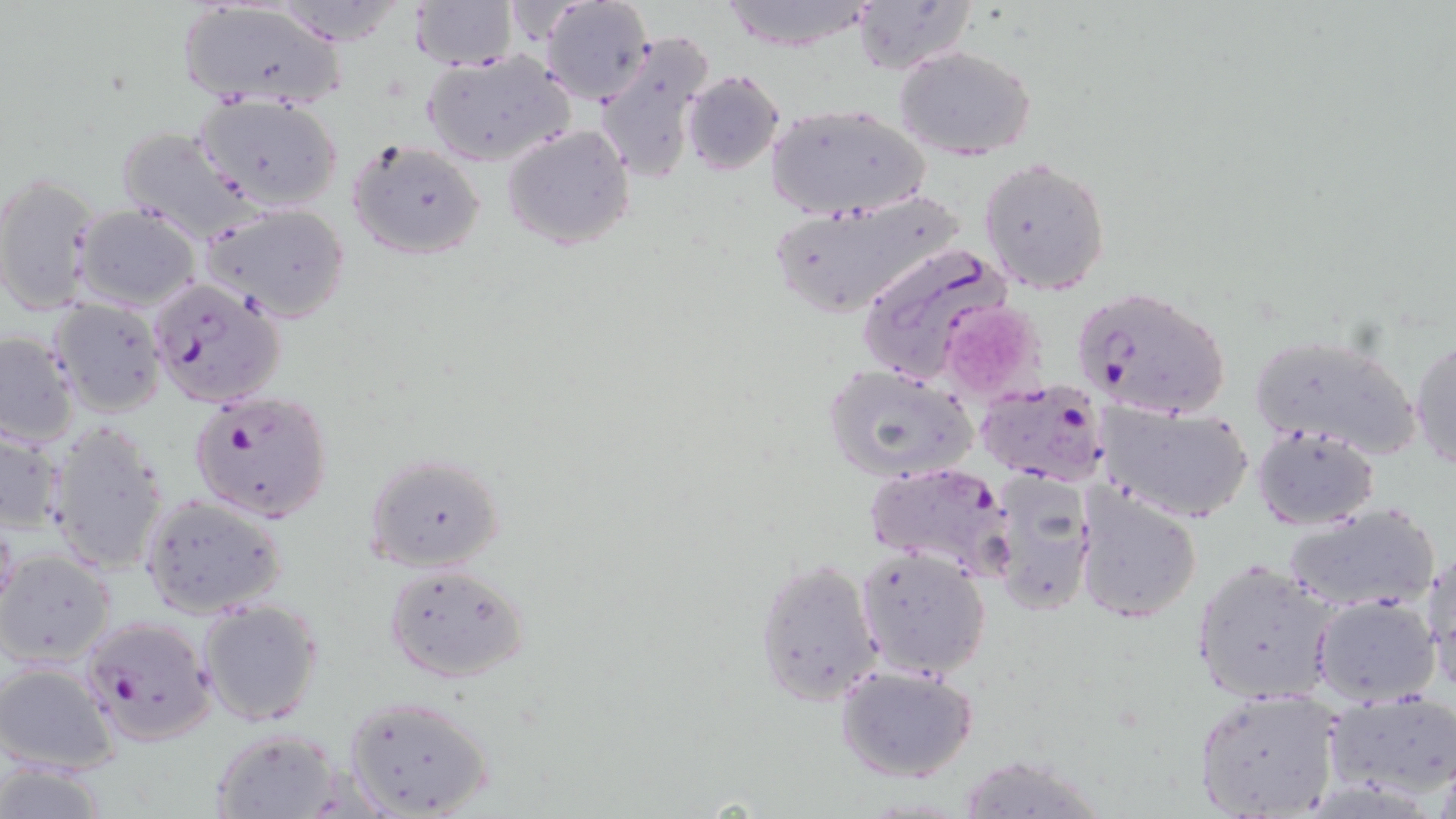 Approximate bounding boxes as [x1, y1, x2, y2] in pixels. Plasmodium falciparum-infected red blood cell locations: [855, 243, 1016, 392], [146, 277, 285, 409], [1073, 285, 1231, 423], [977, 379, 1111, 488], [189, 388, 334, 524], [864, 463, 1017, 581], [76, 615, 217, 745]. Platelet locations: [939, 299, 1049, 402]. Uninfected red blood cell locations: [269, 0, 411, 48], [539, 0, 654, 105], [719, 0, 875, 52], [174, 1, 347, 110], [408, 1, 519, 69], [502, 1, 592, 44], [851, 1, 979, 75], [593, 30, 716, 185], [894, 46, 1037, 161], [421, 49, 575, 168], [680, 70, 785, 175], [197, 94, 344, 210], [765, 104, 929, 221], [502, 124, 636, 251], [114, 126, 259, 242], [346, 138, 486, 262], [978, 158, 1111, 297], [0, 171, 98, 317], [763, 189, 966, 320], [200, 202, 352, 324], [73, 204, 201, 311], [47, 298, 167, 418], [0, 331, 80, 449], [1248, 333, 1423, 461], [1410, 334, 1456, 473], [820, 363, 979, 484], [1092, 397, 1254, 525], [45, 420, 172, 577], [0, 425, 66, 535], [1251, 427, 1380, 528], [363, 452, 505, 573], [989, 470, 1098, 619], [1074, 483, 1203, 624], [139, 494, 287, 619], [1281, 503, 1442, 617], [0, 515, 21, 626], [854, 546, 991, 680], [1423, 548, 1455, 692], [0, 550, 117, 668], [755, 557, 883, 706], [1191, 559, 1338, 707], [383, 562, 531, 683], [1312, 595, 1441, 705], [197, 597, 325, 728], [0, 660, 122, 776], [834, 664, 979, 783], [1192, 688, 1343, 819], [342, 695, 495, 818], [1326, 695, 1456, 799], [210, 727, 342, 818], [955, 754, 1108, 819], [1, 759, 111, 819]. Slide-level diagnosis: Plasmodium falciparum. Captured at 1000x magnification. Thin blood smear. Image is 1456×819 pixels. Optical microscopy. May-Grünwald-Giemsa-stained preparation. One field of a larger specimen.